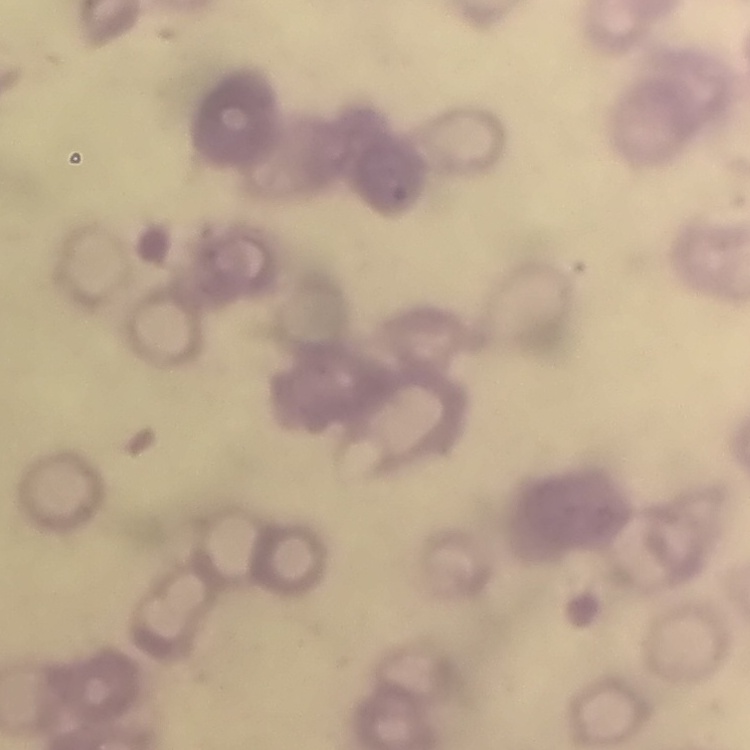

Summary:
  - Erythrocyte morphology: rouleaux formation
  - Image type: square crop of a larger photomicrograph
  - Preparation: thin blood smear
  - Stain: Field's or Giemsa